Give the extent of all Plasmodium falciparum-infected red blood cells.
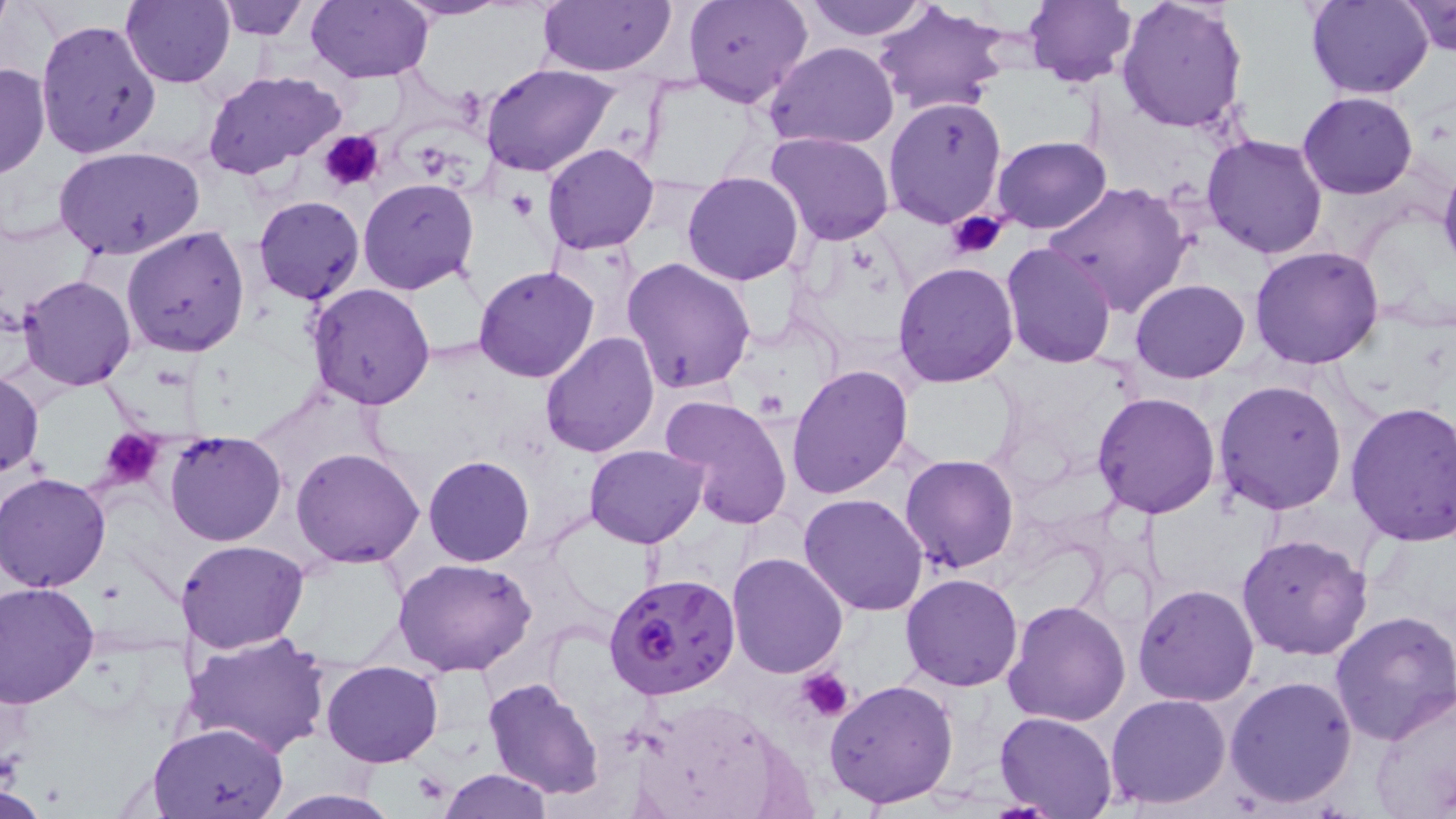

Approximate bounding boxes as named x1/y1/x2/y2 corners in pixels.
Plasmodium falciparum-infected red blood cells: (x1=606, y1=572, x2=739, y2=701).

{
  "slide_level_diagnosis": "Plasmodium falciparum",
  "field_of_view": "one of a larger specimen",
  "modality": "light microscopy",
  "uninfected_red_blood_cell_locations": "approximate bounding boxes as named x1/y1/x2/y2 corners in pixels: (x1=120, y1=0, x2=234, y2=87), (x1=212, y1=0, x2=312, y2=42), (x1=308, y1=0, x2=434, y2=83), (x1=394, y1=0, x2=512, y2=22), (x1=535, y1=0, x2=677, y2=78), (x1=684, y1=0, x2=812, y2=108), (x1=800, y1=0, x2=932, y2=41), (x1=1024, y1=0, x2=1136, y2=87), (x1=1115, y1=0, x2=1250, y2=135), (x1=1304, y1=0, x2=1434, y2=99), (x1=1402, y1=1, x2=1456, y2=55), (x1=871, y1=2, x2=1011, y2=116), (x1=34, y1=20, x2=160, y2=160), (x1=765, y1=41, x2=899, y2=149), (x1=0, y1=61, x2=51, y2=180), (x1=480, y1=62, x2=619, y2=177), (x1=203, y1=71, x2=346, y2=183), (x1=1297, y1=91, x2=1419, y2=199), (x1=882, y1=96, x2=1009, y2=230), (x1=766, y1=131, x2=894, y2=245), (x1=1202, y1=134, x2=1329, y2=259), (x1=989, y1=136, x2=1112, y2=235), (x1=542, y1=143, x2=661, y2=255), (x1=56, y1=147, x2=203, y2=259), (x1=1438, y1=161, x2=1456, y2=273), (x1=681, y1=172, x2=804, y2=287), (x1=358, y1=178, x2=481, y2=295), (x1=1044, y1=180, x2=1192, y2=319), (x1=253, y1=195, x2=365, y2=304), (x1=122, y1=225, x2=251, y2=358), (x1=1000, y1=241, x2=1119, y2=367), (x1=1251, y1=245, x2=1386, y2=369), (x1=622, y1=258, x2=757, y2=394), (x1=892, y1=262, x2=1020, y2=386), (x1=473, y1=265, x2=600, y2=383), (x1=19, y1=274, x2=136, y2=390), (x1=1130, y1=279, x2=1249, y2=383), (x1=306, y1=284, x2=437, y2=409), (x1=539, y1=332, x2=661, y2=459), (x1=787, y1=366, x2=914, y2=500), (x1=0, y1=367, x2=45, y2=481), (x1=1212, y1=379, x2=1347, y2=515), (x1=1092, y1=391, x2=1223, y2=518), (x1=659, y1=393, x2=796, y2=530), (x1=1345, y1=401, x2=1456, y2=546), (x1=165, y1=431, x2=288, y2=546), (x1=585, y1=443, x2=707, y2=547), (x1=292, y1=447, x2=425, y2=567), (x1=900, y1=454, x2=1018, y2=573), (x1=424, y1=455, x2=534, y2=567), (x1=2, y1=471, x2=114, y2=591), (x1=799, y1=492, x2=929, y2=615), (x1=1236, y1=533, x2=1372, y2=660), (x1=175, y1=540, x2=308, y2=653), (x1=727, y1=551, x2=850, y2=678), (x1=394, y1=560, x2=537, y2=677), (x1=900, y1=572, x2=1024, y2=692), (x1=0, y1=581, x2=100, y2=707), (x1=1133, y1=582, x2=1260, y2=706), (x1=1002, y1=597, x2=1132, y2=726), (x1=1330, y1=608, x2=1456, y2=745), (x1=180, y1=630, x2=331, y2=757), (x1=321, y1=660, x2=444, y2=768), (x1=1225, y1=674, x2=1358, y2=809), (x1=484, y1=676, x2=606, y2=800), (x1=825, y1=677, x2=960, y2=810), (x1=1370, y1=687, x2=1456, y2=819), (x1=1105, y1=694, x2=1231, y2=809), (x1=994, y1=711, x2=1118, y2=816), (x1=148, y1=722, x2=289, y2=819), (x1=439, y1=769, x2=551, y2=818), (x1=262, y1=790, x2=406, y2=819)",
  "platelet_locations": "approximate bounding boxes as named x1/y1/x2/y2 corners in pixels: (x1=319, y1=131, x2=383, y2=192), (x1=507, y1=189, x2=537, y2=223), (x1=948, y1=210, x2=1009, y2=261), (x1=99, y1=429, x2=164, y2=487), (x1=798, y1=669, x2=854, y2=721)",
  "preparation": "thin blood smear",
  "stain": "May-Grünwald-Giemsa",
  "image_size": "1456×819 pixels",
  "magnification": "1000x"
}